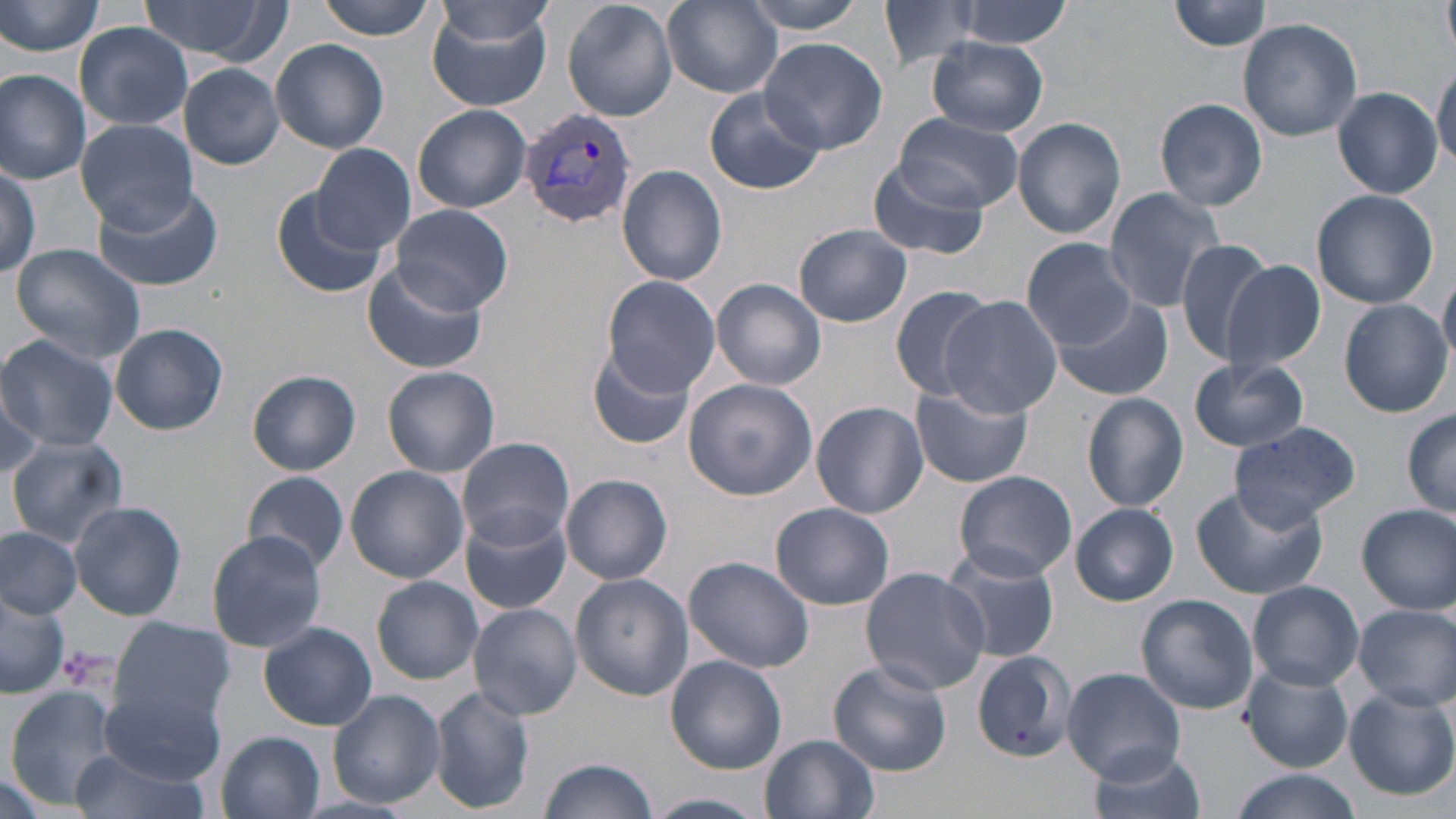 Approximate bounding boxes as named x1/y1/x2/y2 corners in pixels. Uninfected red blood cell locations: (x1=316, y1=0, x2=439, y2=40), (x1=562, y1=0, x2=679, y2=121), (x1=742, y1=0, x2=874, y2=32), (x1=876, y1=0, x2=989, y2=70), (x1=952, y1=0, x2=1074, y2=49), (x1=1442, y1=0, x2=1456, y2=61), (x1=0, y1=1, x2=108, y2=58), (x1=136, y1=1, x2=289, y2=64), (x1=663, y1=1, x2=782, y2=96), (x1=1169, y1=1, x2=1274, y2=52), (x1=426, y1=4, x2=556, y2=114), (x1=437, y1=4, x2=556, y2=49), (x1=1237, y1=19, x2=1363, y2=141), (x1=75, y1=22, x2=193, y2=129), (x1=760, y1=37, x2=887, y2=155), (x1=270, y1=38, x2=389, y2=153), (x1=927, y1=38, x2=1048, y2=136), (x1=179, y1=63, x2=285, y2=169), (x1=1431, y1=64, x2=1455, y2=173), (x1=0, y1=69, x2=90, y2=184), (x1=704, y1=87, x2=825, y2=196), (x1=1333, y1=87, x2=1443, y2=198), (x1=1154, y1=97, x2=1267, y2=211), (x1=412, y1=105, x2=532, y2=213), (x1=892, y1=112, x2=1021, y2=213), (x1=1012, y1=116, x2=1127, y2=241), (x1=75, y1=118, x2=197, y2=230), (x1=312, y1=143, x2=417, y2=254), (x1=868, y1=158, x2=989, y2=262), (x1=0, y1=159, x2=43, y2=279), (x1=617, y1=165, x2=727, y2=286), (x1=90, y1=180, x2=220, y2=291), (x1=272, y1=184, x2=392, y2=300), (x1=1102, y1=188, x2=1229, y2=314), (x1=1311, y1=189, x2=1440, y2=310), (x1=390, y1=203, x2=513, y2=314), (x1=793, y1=223, x2=911, y2=326), (x1=1023, y1=238, x2=1135, y2=348), (x1=1173, y1=239, x2=1278, y2=365), (x1=7, y1=241, x2=148, y2=363), (x1=1220, y1=259, x2=1328, y2=376), (x1=361, y1=260, x2=488, y2=375), (x1=1439, y1=274, x2=1456, y2=368), (x1=600, y1=275, x2=721, y2=394), (x1=712, y1=279, x2=826, y2=389), (x1=889, y1=285, x2=999, y2=400), (x1=1050, y1=295, x2=1172, y2=400), (x1=938, y1=296, x2=1063, y2=418), (x1=1338, y1=299, x2=1452, y2=417), (x1=110, y1=322, x2=228, y2=436), (x1=0, y1=335, x2=118, y2=452), (x1=587, y1=344, x2=698, y2=452), (x1=1188, y1=358, x2=1310, y2=452), (x1=382, y1=366, x2=500, y2=477), (x1=247, y1=370, x2=360, y2=474), (x1=683, y1=379, x2=817, y2=500), (x1=910, y1=385, x2=1032, y2=488), (x1=0, y1=386, x2=45, y2=478), (x1=1082, y1=392, x2=1190, y2=513), (x1=811, y1=401, x2=929, y2=518), (x1=1401, y1=409, x2=1456, y2=518), (x1=1229, y1=423, x2=1360, y2=527), (x1=456, y1=436, x2=575, y2=550), (x1=6, y1=437, x2=129, y2=548), (x1=345, y1=466, x2=469, y2=583), (x1=242, y1=471, x2=351, y2=575), (x1=953, y1=472, x2=1077, y2=582), (x1=561, y1=474, x2=673, y2=584), (x1=1192, y1=485, x2=1327, y2=600), (x1=68, y1=500, x2=186, y2=621), (x1=770, y1=502, x2=895, y2=610), (x1=1357, y1=503, x2=1456, y2=614), (x1=1071, y1=504, x2=1178, y2=605), (x1=460, y1=509, x2=572, y2=615), (x1=0, y1=526, x2=81, y2=620), (x1=205, y1=531, x2=328, y2=651), (x1=942, y1=547, x2=1059, y2=663), (x1=683, y1=555, x2=815, y2=673), (x1=859, y1=566, x2=989, y2=694), (x1=570, y1=574, x2=692, y2=699), (x1=372, y1=576, x2=484, y2=685), (x1=1248, y1=581, x2=1362, y2=690), (x1=0, y1=588, x2=71, y2=698), (x1=1136, y1=594, x2=1258, y2=715), (x1=467, y1=603, x2=583, y2=721), (x1=1351, y1=604, x2=1456, y2=709), (x1=110, y1=618, x2=234, y2=729), (x1=258, y1=621, x2=377, y2=731), (x1=970, y1=651, x2=1077, y2=761), (x1=665, y1=655, x2=787, y2=773), (x1=829, y1=661, x2=951, y2=776), (x1=1242, y1=664, x2=1352, y2=771), (x1=1060, y1=667, x2=1185, y2=783), (x1=96, y1=685, x2=223, y2=787), (x1=429, y1=686, x2=534, y2=813), (x1=6, y1=687, x2=119, y2=806), (x1=1345, y1=688, x2=1455, y2=801), (x1=328, y1=689, x2=446, y2=808), (x1=217, y1=732, x2=325, y2=818), (x1=760, y1=734, x2=878, y2=819), (x1=66, y1=745, x2=209, y2=819), (x1=1088, y1=748, x2=1207, y2=819), (x1=540, y1=757, x2=658, y2=818), (x1=0, y1=767, x2=53, y2=819), (x1=1225, y1=770, x2=1364, y2=819), (x1=646, y1=793, x2=766, y2=819). Plasmodium vivax-infected red blood cell locations: (x1=518, y1=107, x2=638, y2=230). Platelet locations: (x1=55, y1=646, x2=108, y2=690). Slide-level diagnosis: Plasmodium vivax. One field of a larger specimen. May-Grünwald-Giemsa stain. 1000x magnification. Image is 1456×819 pixels. Thin blood smear. Optical microscopy.